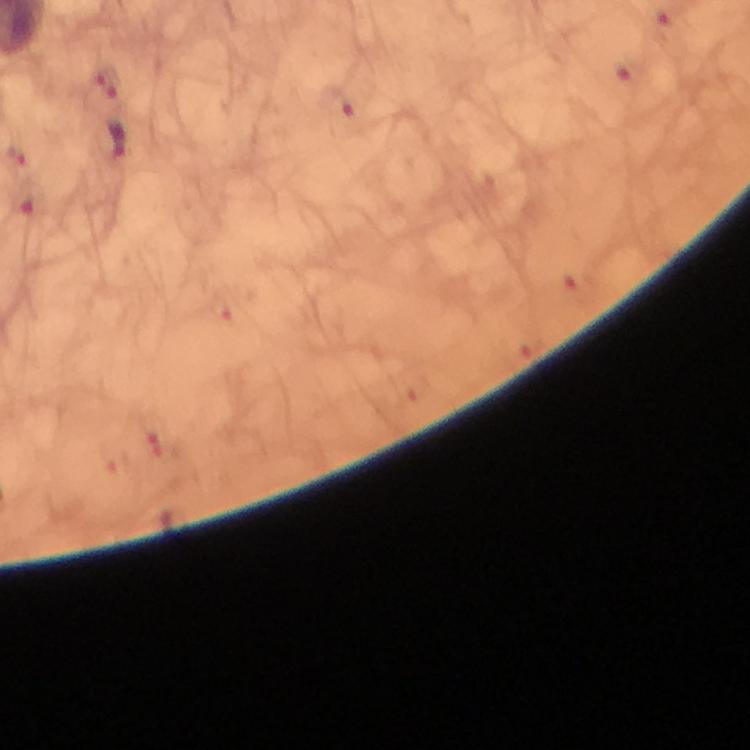

Approximate centers as (x, y) in pixels. Malaria parasite locations: (108, 83), (338, 105), (118, 138), (17, 156), (155, 442). Thick smear. Photographed with a smartphone mounted on the microscope. Immersion oil was used. 100x magnification. Image is 750×750 pixels. Cropped region of a single field of view. Giemsa stain. From a malaria diagnostic workup.